Give the extent of all Babesia divergens-infected red blood cells.
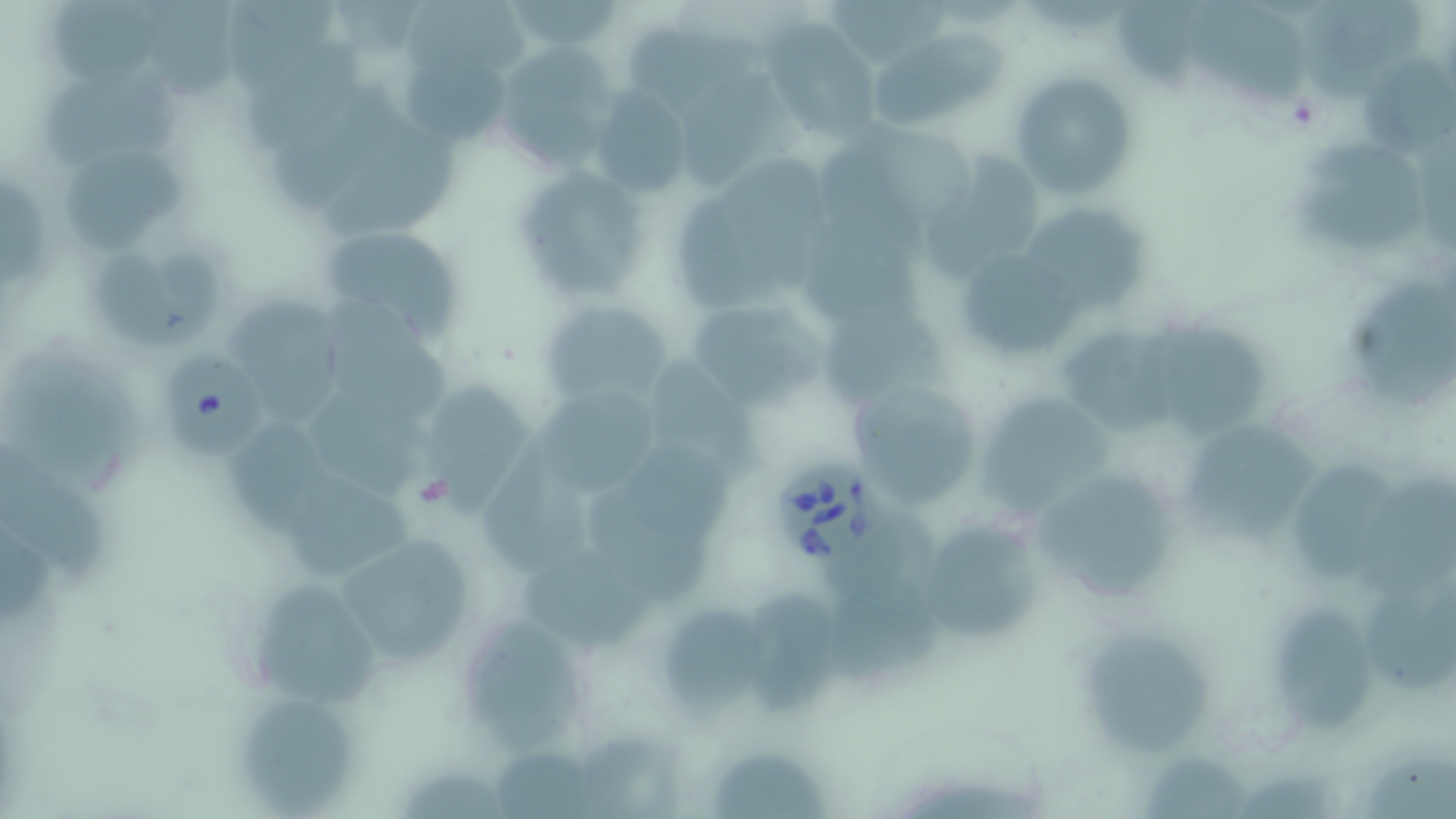

Approximate bounding boxes as (x1, y1, x2, y2) in pixels.
Babesia divergens-infected red blood cells: (161, 354, 270, 454), (771, 457, 885, 566).

Summary:
  - Uninfected red blood cell locations: (57, 0, 158, 90), (154, 0, 235, 102), (515, 0, 621, 48), (1182, 1, 1306, 107), (407, 2, 527, 81), (1304, 2, 1423, 105), (831, 3, 955, 63), (1116, 3, 1197, 98), (227, 5, 339, 99), (761, 22, 883, 140), (629, 31, 764, 113), (877, 35, 1006, 127), (248, 41, 360, 152), (494, 44, 621, 171), (1366, 58, 1456, 161), (404, 59, 505, 147), (1010, 71, 1138, 200), (681, 78, 791, 190), (49, 82, 186, 164), (275, 83, 409, 217), (592, 87, 691, 198), (875, 132, 978, 226), (318, 133, 455, 240), (1295, 148, 1427, 249), (67, 158, 186, 249), (721, 159, 837, 290), (927, 159, 1040, 271), (510, 166, 648, 301), (1, 184, 49, 287), (675, 194, 774, 311), (1027, 214, 1146, 305), (804, 221, 921, 326), (316, 223, 464, 339), (952, 247, 1083, 362), (100, 255, 179, 345), (162, 255, 224, 342), (1351, 284, 1456, 404), (683, 294, 824, 412), (538, 299, 673, 406), (226, 301, 340, 429), (325, 302, 453, 424), (1163, 321, 1266, 431), (1066, 334, 1184, 431), (647, 361, 768, 483), (28, 376, 140, 481), (848, 380, 988, 511), (428, 382, 526, 513), (980, 388, 1116, 521), (308, 397, 425, 501), (536, 399, 659, 493), (229, 428, 339, 541), (1188, 432, 1313, 546), (0, 449, 106, 578), (626, 449, 733, 540), (485, 460, 596, 578), (1292, 466, 1396, 578), (1040, 472, 1168, 604), (293, 473, 414, 582), (1362, 477, 1456, 592), (588, 495, 710, 606), (915, 518, 1046, 649), (827, 520, 939, 612), (331, 530, 482, 670), (520, 554, 652, 648), (1367, 581, 1456, 693), (825, 586, 941, 686), (255, 589, 379, 706), (745, 592, 838, 716), (1279, 611, 1373, 731), (661, 613, 765, 712), (463, 623, 584, 757), (1084, 639, 1211, 755), (241, 705, 356, 810), (585, 738, 693, 819), (497, 749, 599, 819), (714, 755, 824, 819), (1366, 758, 1456, 819), (1145, 761, 1247, 812)
  - Slide-level diagnosis: Babesia divergens
  - Image size: 1456×819 pixels
  - Field of view: one of a larger specimen
  - Stain: May-Grünwald-Giemsa
  - Preparation: thin blood smear
  - Modality: optical microscopy
  - Magnification: 1000x